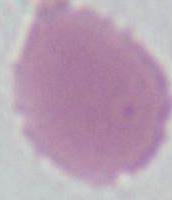

Photomicrograph. 1000x magnification. An erythrocyte is shown.